Report the malaria status of this cell.
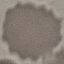

Uninfected.

Summary:
  - Image type: automatically extracted cell patch, resized to 64 × 64 pixels
  - Stain: Giemsa
  - Capture: smartphone camera at the microscope eyepiece
  - Preparation: thin blood film